Report the malaria status of this cell.
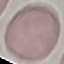

Uninfected.

Summary:
  - Stain: Giemsa
  - Image type: automatically extracted cell patch, resized to 64 × 64 pixels
  - Capture: smartphone camera at the microscope eyepiece
  - Preparation: thin blood smear